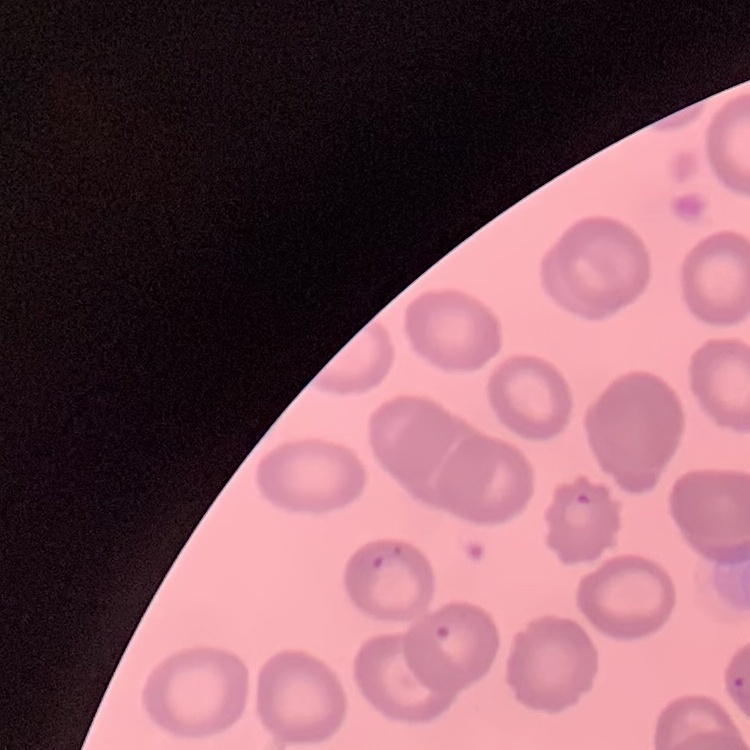
red blood cell morphology = no rouleaux formation
preparation = thin blood film
image type = square crop of a larger photomicrograph
stain = Field's or Giemsa